Describe the morphology of the red blood cells.
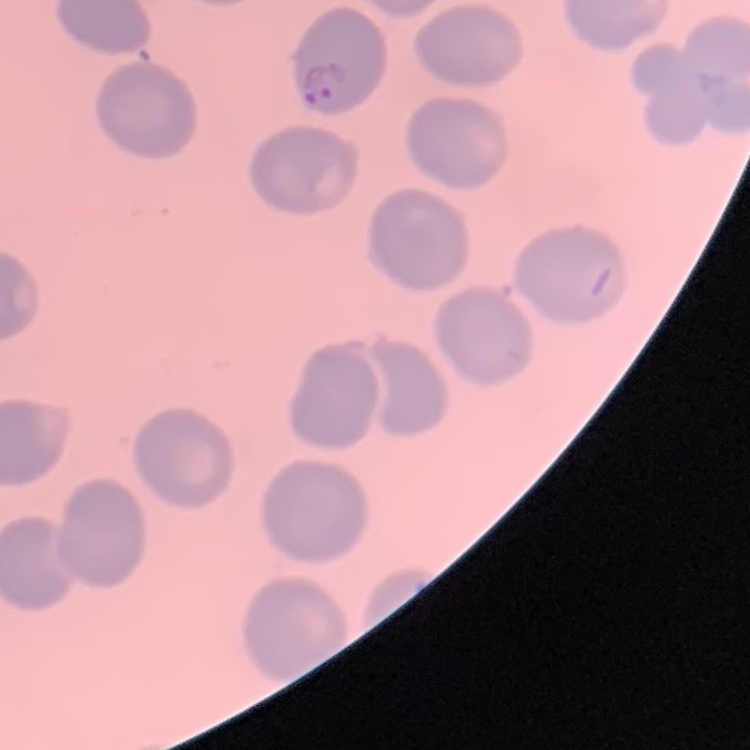
No rouleaux formation.

preparation: thin peripheral smear
stain: Field's or Giemsa
image_type: square crop of a larger photomicrograph